Classify this cell by malaria status.
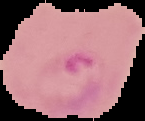

It is parasitized.

Image is 145×121 pixels. From a thin blood smear. Cell region segmented out of the field of view; the surrounding area is masked to black.